Identify the parasite.
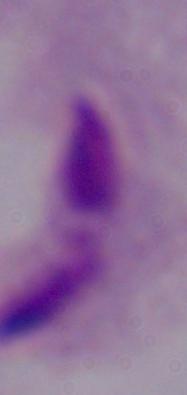
This is a trichomonad.

{
  "modality": "micrograph",
  "magnification": "1000x"
}